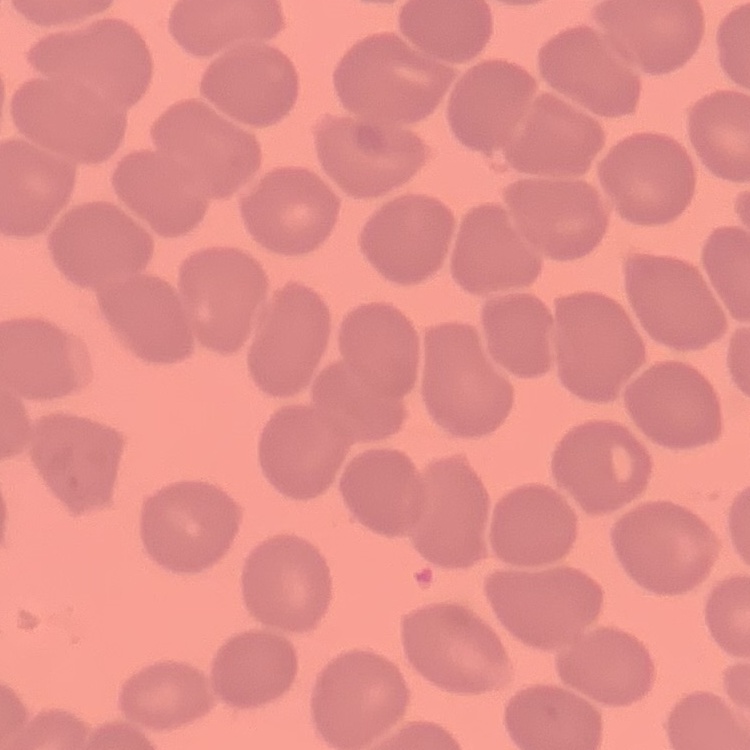

{
  "red_blood_cell_morphology": "no rouleaux formation",
  "image_type": "one tile cut from a larger photomicrograph",
  "preparation": "thin blood film",
  "stain": "Field's or Giemsa"
}